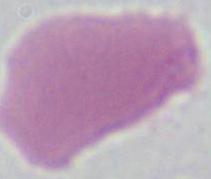
Photomicrograph. 1000x magnification. An erythrocyte is shown.